Outline each Plasmodium falciparum-infected red blood cell.
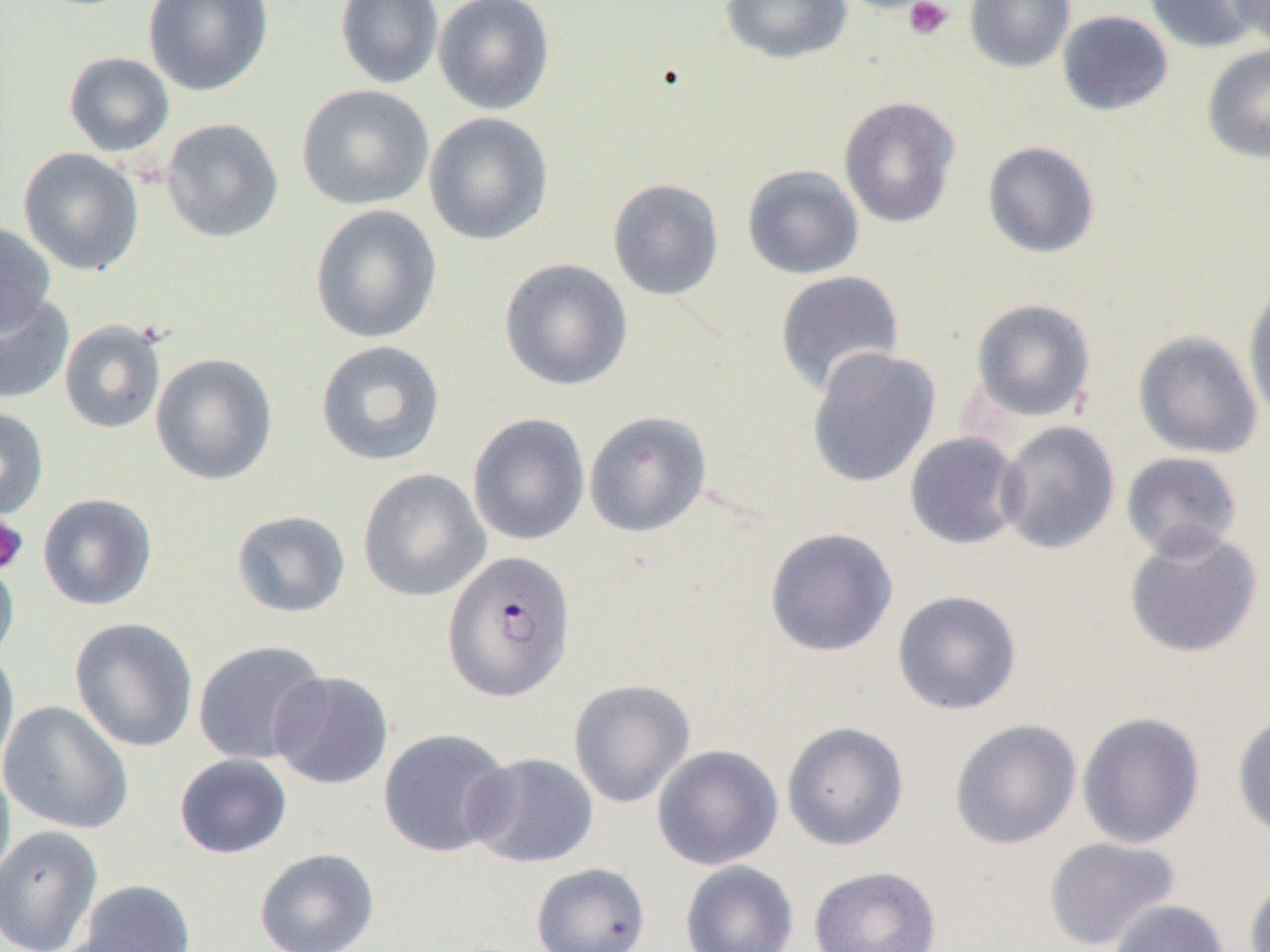
Approximate bounding boxes as (x1, y1, x2, y2) in pixels.
Plasmodium falciparum-infected red blood cells: (442, 549, 576, 703).

Summary:
  - Uninfected red blood cell locations: (143, 0, 273, 96), (335, 0, 444, 89), (433, 0, 555, 115), (721, 0, 852, 64), (964, 0, 1075, 73), (1144, 0, 1263, 53), (1226, 0, 1270, 51), (1057, 10, 1173, 116), (1201, 44, 1270, 164), (63, 52, 174, 157), (296, 84, 434, 211), (838, 96, 961, 229), (423, 111, 555, 246), (160, 117, 284, 244), (982, 141, 1100, 258), (17, 147, 144, 276), (742, 164, 864, 280), (607, 178, 725, 301), (310, 204, 443, 344), (0, 222, 56, 335), (499, 257, 633, 391), (774, 270, 905, 396), (1243, 283, 1270, 422), (0, 290, 74, 404), (971, 298, 1096, 422), (59, 320, 167, 434), (1133, 330, 1263, 459), (315, 340, 446, 467), (806, 347, 941, 488), (150, 353, 278, 486), (0, 406, 49, 521), (584, 411, 712, 538), (467, 413, 590, 546), (996, 421, 1119, 555), (904, 432, 1026, 550), (1121, 452, 1243, 560), (357, 468, 490, 603), (37, 493, 157, 611), (230, 510, 351, 618), (764, 527, 898, 657), (1124, 528, 1264, 659), (0, 550, 20, 666), (892, 590, 1022, 715), (69, 617, 198, 753), (192, 640, 327, 765), (0, 646, 20, 777), (269, 670, 393, 791), (568, 679, 695, 808), (0, 701, 134, 835), (1232, 710, 1270, 844), (1077, 712, 1206, 849), (950, 718, 1082, 849), (781, 721, 909, 851), (378, 727, 514, 858), (651, 744, 783, 870), (464, 752, 599, 868), (174, 754, 293, 859), (0, 759, 16, 889), (0, 824, 103, 952), (1043, 836, 1180, 950), (254, 847, 380, 952), (680, 860, 799, 952), (530, 862, 650, 952), (808, 865, 941, 952), (1243, 875, 1270, 952), (77, 879, 196, 952), (1109, 898, 1230, 952)
  - Platelet locations: (904, 0, 953, 41), (0, 515, 29, 575)
  - Slide-level diagnosis: Plasmodium falciparum
  - Image size: 1270×952 pixels
  - Field of view: one of a larger specimen
  - Preparation: thin blood smear
  - Magnification: 1000x
  - Modality: light microscopy